Assess for parasitized red blood cells.
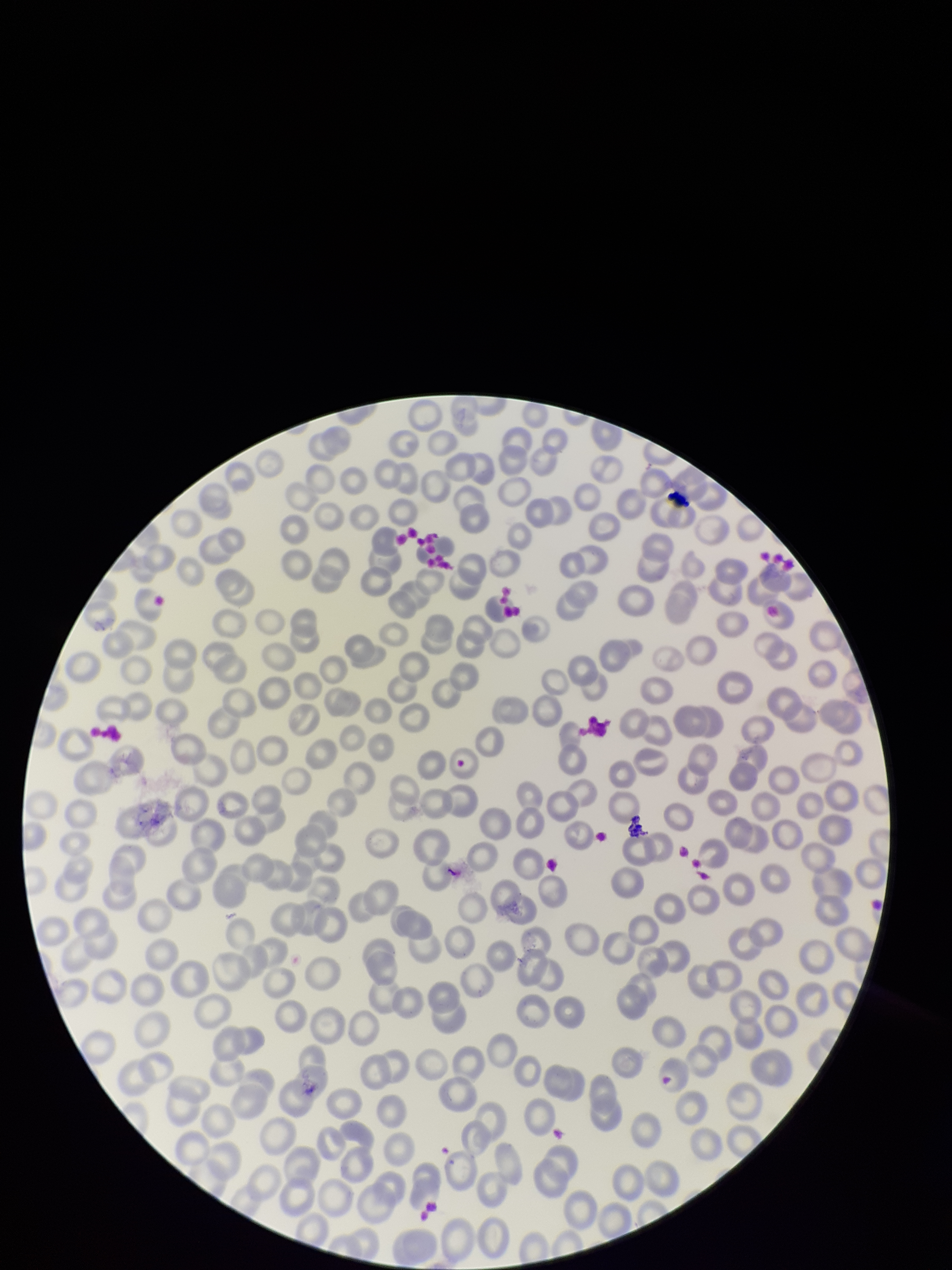

None identified.

Summary:
  - Parasitized red blood cell count: 0
  - Capture: smartphone photograph through the microscope eyepiece
  - Image size: 952×1270 pixels
  - Patient malaria status: negative
  - Field of view: single
  - Red blood cell count: 228
  - Stain: Giemsa
  - Preparation: thin smear